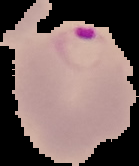

Summary:
  - Image size: 139×166 pixels
  - Image type: segmented cell region with the area outside set to black
  - Preparation: thin blood film
  - Malaria status: parasitized